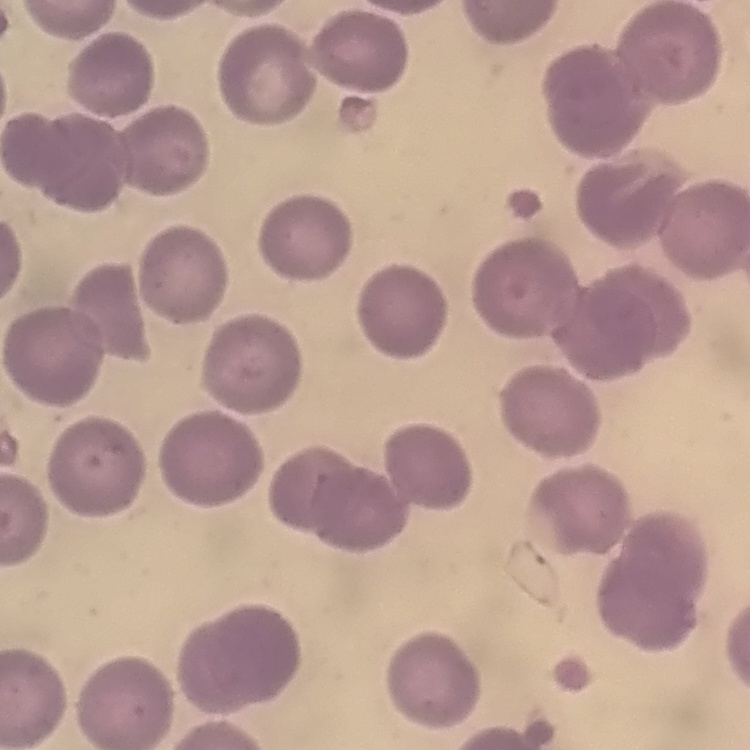

erythrocyte morphology = no rouleaux formation
image type = square crop of a larger photomicrograph
stain = Field's or Giemsa
preparation = thin peripheral smear